Assess this cell for malaria.
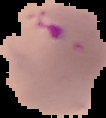
Parasitized.

Summary:
  - Image size: 106×118 pixels
  - Preparation: thin blood film
  - Image type: segmented cell region on a black background